Give the preparation type.
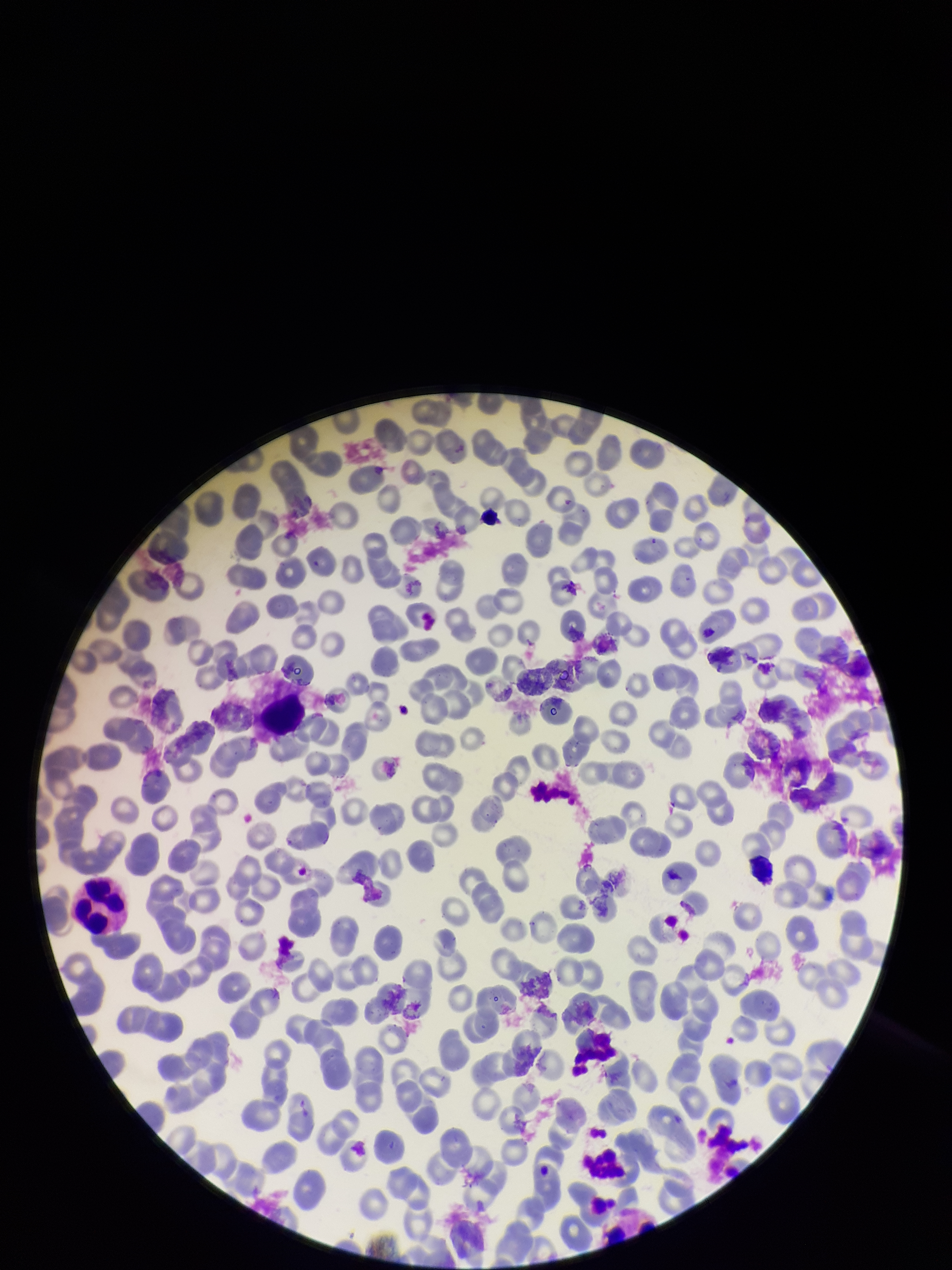

It is a thin blood smear.

Single field of view. Patient malaria status: negative. Red blood cell count: 244. Parasitized red blood cells: none detected. Image is 952×1270 pixels. Stained with Giemsa. Photographed through the microscope eyepiece with a smartphone camera. Parasitized red blood cell count: 0.